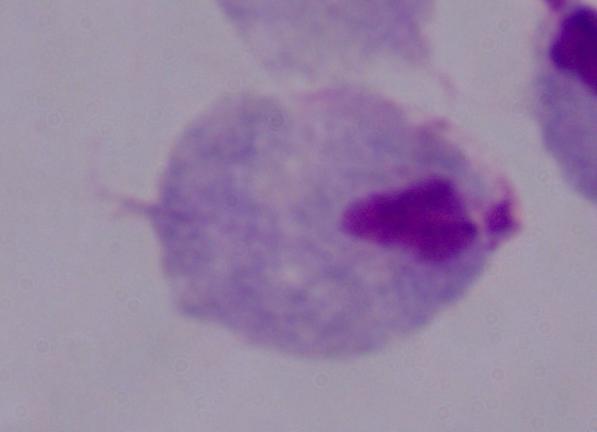 Photomicrograph. 1000x magnification. A trichomonad is shown.